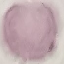
Result: no malaria parasites detected. Cell patch, automatically extracted from a larger field of view and resized to 64 × 64 pixels. Giemsa-stained preparation. Thin smear of blood. Acquired by smartphone through the microscope eyepiece.